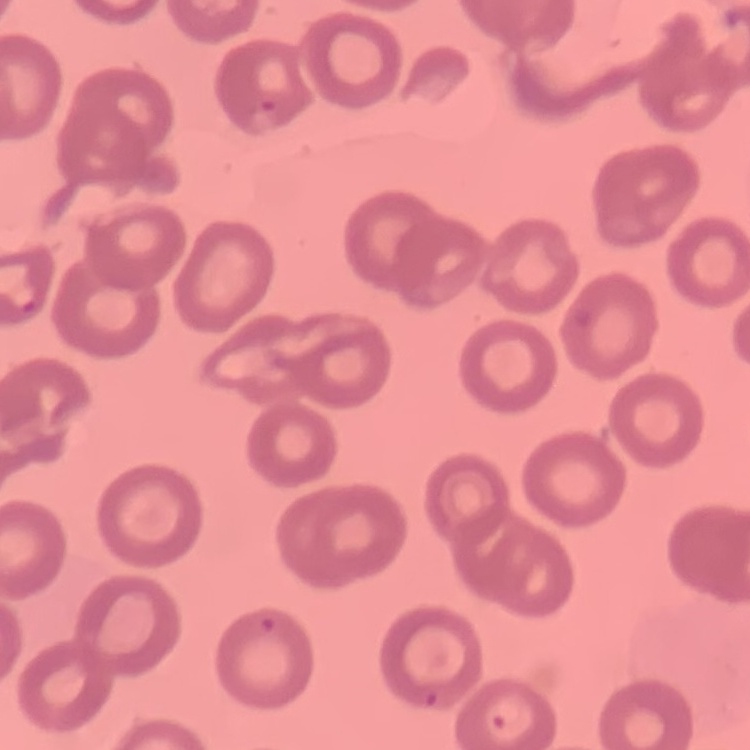
The erythrocytes exhibit no rouleaux formation. Thin blood smear. One tile cut from a larger photomicrograph. Field's or Giemsa stain.